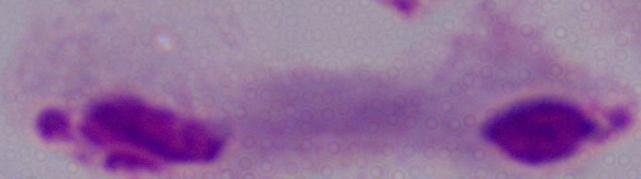

identification = trichomonad
magnification = 1000x
modality = photomicrograph